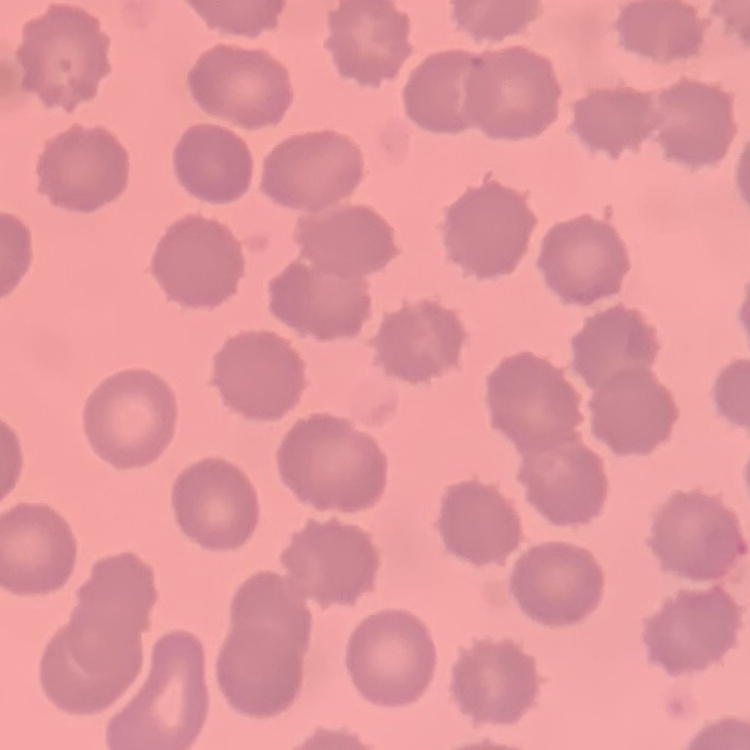
red blood cell morphology = no rouleaux formation
stain = Field's or Giemsa
preparation = thin blood film
image type = square crop of a larger photomicrograph